Classify this cell by malaria status.
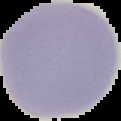

It is uninfected.

Summary:
  - Image size: 121×121 pixels
  - Image type: cell region segmented out of the field of view; surrounding area masked to black
  - Preparation: thin blood smear